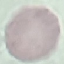

Summary:
  - Malaria status: uninfected
  - Preparation: thin blood smear
  - Capture: smartphone camera at the microscope eyepiece
  - Stain: Giemsa
  - Image type: automatically extracted cell patch, resized to 64 × 64 pixels